Classify this cell by malaria status.
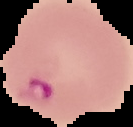

It is parasitized.

Image is 133×127 pixels. Cell region segmented out of the field of view; the surrounding area is masked to black. From a thin blood smear.